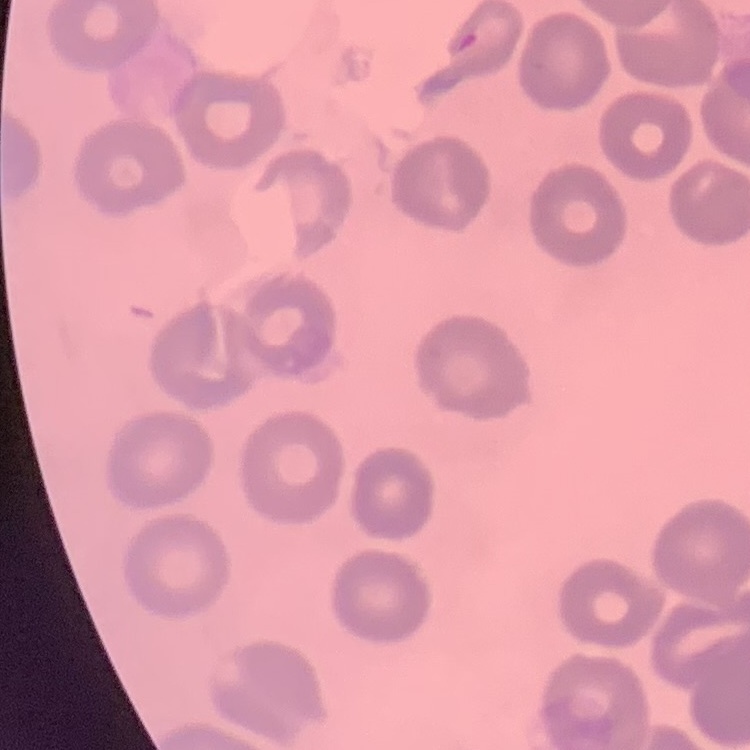 The erythrocytes exhibit no rouleaux formation. Stained with either Field's or Giemsa. One tile cut from a larger photomicrograph. Thin blood film.